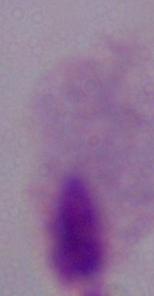

Photomicrograph. A trichomonad is shown. 1000x magnification.